State which parasite is depicted.
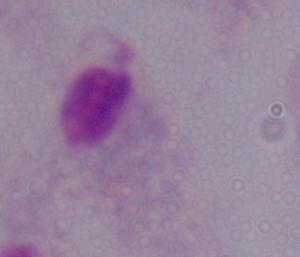
A trichomonad.

Captured at 1000x magnification. Photomicrograph.